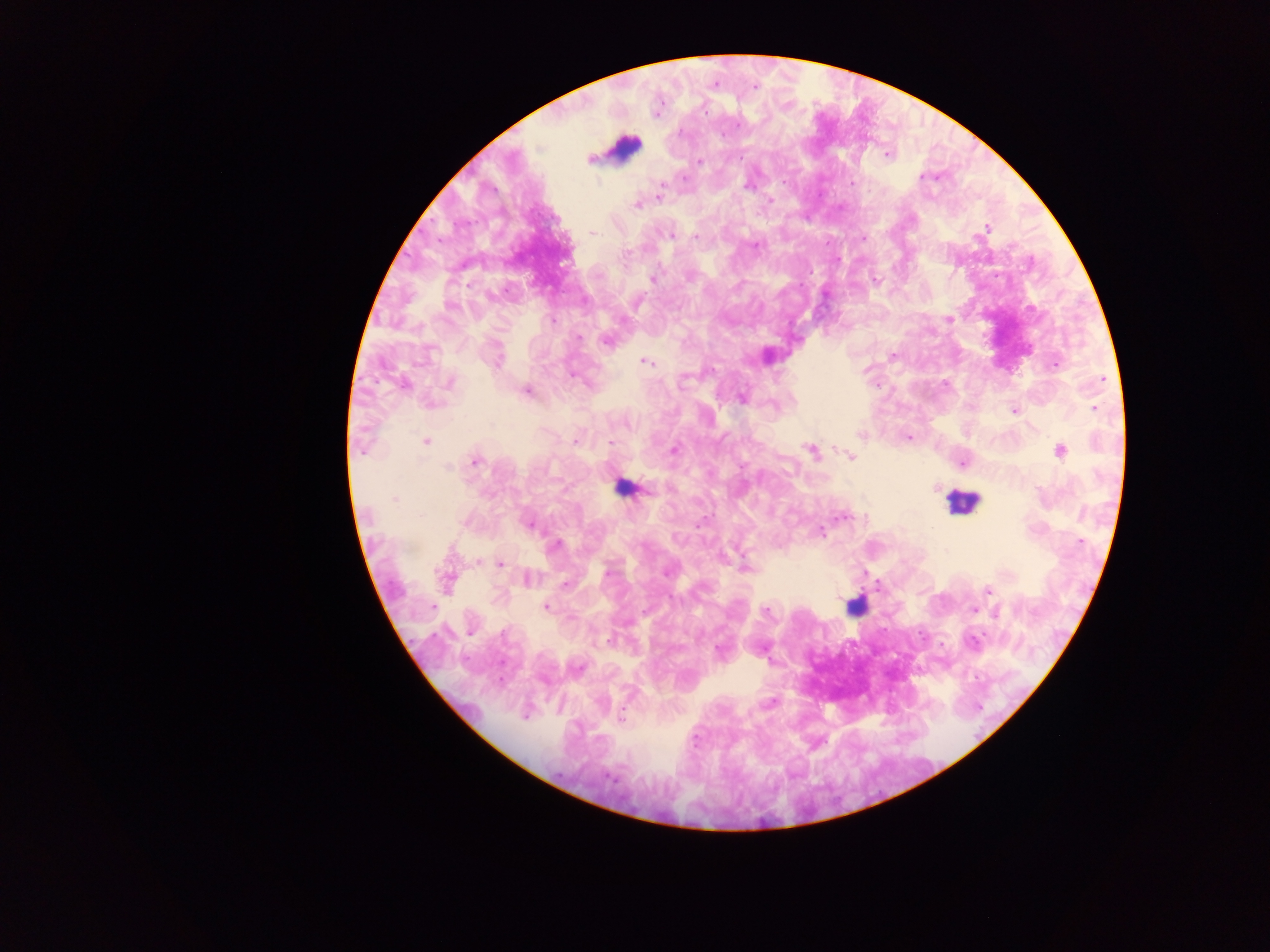
Approximate centers as {x, y} in pixels.
Summary:
  - Plasmodium parasite locations: {755, 87}, {704, 111}, {737, 126}, {887, 155}, {591, 160}, {699, 161}, {923, 176}, {684, 177}, {664, 181}, {852, 183}, {659, 196}, {770, 200}, {636, 206}, {986, 228}, {593, 232}, {671, 236}, {696, 237}, {863, 238}, {754, 246}, {653, 279}, {875, 281}, {449, 307}, {949, 319}, {552, 321}, {577, 337}, {606, 341}, {893, 357}, {498, 361}, {645, 362}, {1054, 364}, {1103, 379}, {450, 383}, {402, 385}, {526, 390}, {742, 399}, {431, 405}, {1094, 408}, {1014, 411}, {860, 434}, {909, 438}, {426, 442}, {574, 442}, {609, 443}, {362, 451}, {673, 451}, {812, 451}, {1060, 451}, {851, 457}, {475, 461}, {963, 463}, {449, 467}, {395, 499}, {843, 517}, {529, 525}, {821, 532}, {1081, 542}, {555, 546}, {480, 562}, {499, 564}, {747, 568}, {608, 572}, {666, 573}, {528, 580}, {565, 585}, {988, 590}, {432, 607}, {545, 607}, {973, 610}, {767, 611}, {997, 613}, {471, 633}, {609, 641}, {973, 642}, {719, 651}, {578, 667}, {771, 703}, {524, 716}, {621, 718}, {695, 740}
  - Leukocyte locations: {624, 147}, {619, 487}, {962, 503}, {854, 607}
  - Field of view: single
  - Capture: mobile-phone photograph through a microscope
  - Country: Ghana
  - Preparation: thick blood smear
  - Image size: 1270×952 pixels